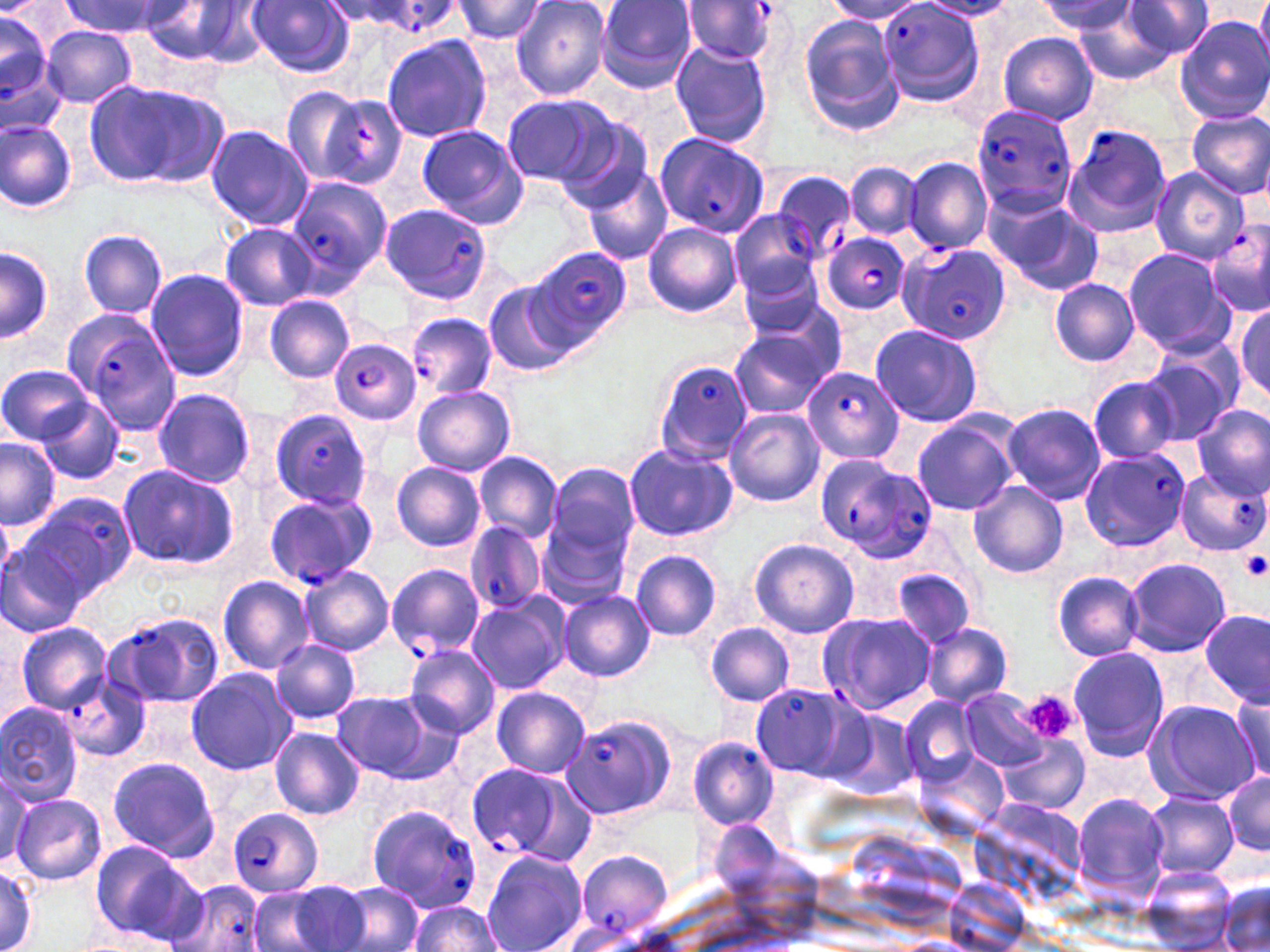
Summary:
  - Coordinate format: approximate bounding boxes as named x1/y1/x2/y2 corners in pixels
  - Platelet locations: (x1=1241, y1=552, x2=1269, y2=584), (x1=1021, y1=691, x2=1080, y2=743)
  - Plasmodium falciparum-infected red blood cell locations: (x1=678, y1=2, x2=780, y2=65), (x1=877, y1=4, x2=986, y2=107), (x1=0, y1=14, x2=52, y2=104), (x1=972, y1=103, x2=1077, y2=217), (x1=1061, y1=123, x2=1174, y2=238), (x1=653, y1=132, x2=769, y2=238), (x1=769, y1=169, x2=856, y2=262), (x1=283, y1=175, x2=391, y2=289), (x1=377, y1=204, x2=491, y2=304), (x1=1203, y1=219, x2=1270, y2=318), (x1=821, y1=231, x2=910, y2=315), (x1=898, y1=243, x2=1011, y2=342), (x1=531, y1=246, x2=633, y2=344), (x1=53, y1=310, x2=178, y2=433), (x1=394, y1=314, x2=498, y2=405), (x1=329, y1=338, x2=420, y2=425), (x1=651, y1=358, x2=753, y2=464), (x1=802, y1=366, x2=905, y2=464), (x1=269, y1=408, x2=374, y2=510), (x1=1079, y1=445, x2=1189, y2=551), (x1=819, y1=457, x2=936, y2=561), (x1=1177, y1=468, x2=1267, y2=556), (x1=263, y1=491, x2=378, y2=589), (x1=466, y1=523, x2=545, y2=615), (x1=386, y1=564, x2=483, y2=658), (x1=104, y1=611, x2=225, y2=710), (x1=63, y1=675, x2=151, y2=763), (x1=750, y1=683, x2=854, y2=779), (x1=563, y1=714, x2=677, y2=820), (x1=689, y1=737, x2=779, y2=830), (x1=465, y1=761, x2=584, y2=865), (x1=365, y1=803, x2=484, y2=916), (x1=227, y1=807, x2=324, y2=898), (x1=572, y1=849, x2=672, y2=941), (x1=169, y1=880, x2=270, y2=952)
  - Uninfected red blood cell locations: (x1=336, y1=0, x2=462, y2=42), (x1=448, y1=0, x2=550, y2=44), (x1=596, y1=0, x2=698, y2=94), (x1=1122, y1=0, x2=1212, y2=62), (x1=1253, y1=0, x2=1270, y2=76), (x1=62, y1=1, x2=173, y2=37), (x1=246, y1=1, x2=355, y2=77), (x1=511, y1=1, x2=612, y2=100), (x1=824, y1=1, x2=926, y2=25), (x1=1039, y1=1, x2=1135, y2=34), (x1=141, y1=3, x2=246, y2=65), (x1=194, y1=3, x2=272, y2=68), (x1=318, y1=3, x2=430, y2=31), (x1=1072, y1=4, x2=1188, y2=85), (x1=797, y1=16, x2=904, y2=136), (x1=1175, y1=16, x2=1270, y2=124), (x1=43, y1=27, x2=136, y2=108), (x1=0, y1=31, x2=66, y2=140), (x1=997, y1=33, x2=1100, y2=124), (x1=380, y1=34, x2=492, y2=143), (x1=669, y1=41, x2=772, y2=149), (x1=86, y1=78, x2=230, y2=190), (x1=283, y1=85, x2=370, y2=185), (x1=501, y1=92, x2=617, y2=189), (x1=1186, y1=111, x2=1270, y2=200), (x1=553, y1=114, x2=655, y2=213), (x1=1, y1=119, x2=77, y2=212), (x1=416, y1=124, x2=528, y2=229), (x1=204, y1=125, x2=313, y2=232), (x1=903, y1=155, x2=991, y2=255), (x1=846, y1=161, x2=922, y2=241), (x1=584, y1=165, x2=673, y2=265), (x1=1150, y1=167, x2=1248, y2=262), (x1=987, y1=190, x2=1100, y2=294), (x1=729, y1=210, x2=824, y2=299), (x1=643, y1=222, x2=742, y2=318), (x1=220, y1=223, x2=318, y2=309), (x1=78, y1=228, x2=168, y2=321), (x1=1, y1=245, x2=52, y2=344), (x1=1123, y1=248, x2=1237, y2=358), (x1=734, y1=257, x2=832, y2=345), (x1=144, y1=268, x2=251, y2=382), (x1=1049, y1=278, x2=1140, y2=367), (x1=481, y1=280, x2=581, y2=378), (x1=740, y1=289, x2=848, y2=382), (x1=263, y1=295, x2=354, y2=384), (x1=1235, y1=305, x2=1268, y2=399), (x1=869, y1=324, x2=984, y2=427), (x1=727, y1=327, x2=834, y2=418), (x1=1139, y1=348, x2=1239, y2=445), (x1=0, y1=364, x2=93, y2=444), (x1=1087, y1=377, x2=1180, y2=464), (x1=412, y1=385, x2=515, y2=476), (x1=152, y1=387, x2=256, y2=487), (x1=35, y1=400, x2=124, y2=484), (x1=1003, y1=402, x2=1107, y2=503), (x1=1192, y1=406, x2=1269, y2=501), (x1=724, y1=408, x2=823, y2=507), (x1=911, y1=414, x2=1022, y2=516), (x1=0, y1=440, x2=60, y2=530), (x1=623, y1=443, x2=736, y2=542), (x1=475, y1=450, x2=562, y2=545), (x1=391, y1=462, x2=486, y2=552), (x1=544, y1=463, x2=640, y2=574), (x1=116, y1=464, x2=239, y2=571), (x1=969, y1=481, x2=1069, y2=579), (x1=25, y1=494, x2=138, y2=596), (x1=0, y1=533, x2=96, y2=641), (x1=749, y1=538, x2=859, y2=638), (x1=631, y1=549, x2=722, y2=641), (x1=1124, y1=557, x2=1231, y2=657), (x1=298, y1=566, x2=394, y2=657), (x1=893, y1=568, x2=974, y2=651), (x1=1052, y1=571, x2=1145, y2=660), (x1=218, y1=576, x2=316, y2=673), (x1=556, y1=588, x2=655, y2=683), (x1=465, y1=592, x2=570, y2=696), (x1=820, y1=611, x2=934, y2=715), (x1=1200, y1=611, x2=1268, y2=706), (x1=14, y1=622, x2=114, y2=715), (x1=706, y1=623, x2=796, y2=705), (x1=922, y1=623, x2=1014, y2=709), (x1=269, y1=639, x2=360, y2=723), (x1=403, y1=643, x2=500, y2=738), (x1=1067, y1=647, x2=1170, y2=762), (x1=185, y1=668, x2=297, y2=775), (x1=491, y1=687, x2=591, y2=779), (x1=331, y1=690, x2=454, y2=784), (x1=958, y1=691, x2=1048, y2=771), (x1=1229, y1=695, x2=1269, y2=783), (x1=901, y1=697, x2=980, y2=784), (x1=0, y1=699, x2=84, y2=805), (x1=1141, y1=699, x2=1260, y2=806), (x1=827, y1=707, x2=920, y2=798), (x1=269, y1=727, x2=364, y2=820), (x1=999, y1=735, x2=1088, y2=814), (x1=913, y1=749, x2=1011, y2=841), (x1=106, y1=757, x2=221, y2=862), (x1=0, y1=767, x2=37, y2=866), (x1=1222, y1=768, x2=1270, y2=859), (x1=1144, y1=791, x2=1240, y2=881), (x1=10, y1=792, x2=107, y2=885), (x1=1071, y1=792, x2=1171, y2=902), (x1=90, y1=840, x2=194, y2=941), (x1=481, y1=850, x2=588, y2=952), (x1=0, y1=865, x2=38, y2=951), (x1=1140, y1=865, x2=1238, y2=949), (x1=280, y1=880, x2=376, y2=951), (x1=338, y1=881, x2=422, y2=952), (x1=1217, y1=881, x2=1270, y2=952), (x1=246, y1=885, x2=337, y2=952), (x1=407, y1=901, x2=503, y2=951)
  - Slide-level diagnosis: Plasmodium falciparum
  - Field of view: one of a larger specimen
  - Preparation: thin blood smear
  - Magnification: 1000x
  - Image size: 1270×952 pixels
  - Modality: light microscopy
  - Stain: May-Grünwald-Giemsa